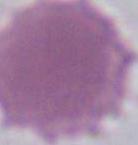

Summary:
  - Identification: erythrocyte
  - Magnification: 1000x
  - Modality: micrograph